Report the malaria status of this cell.
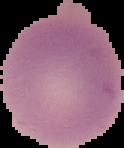

It is uninfected.

From a thin blood film. Image is 124×148 pixels. Segmented cell region on a black background.